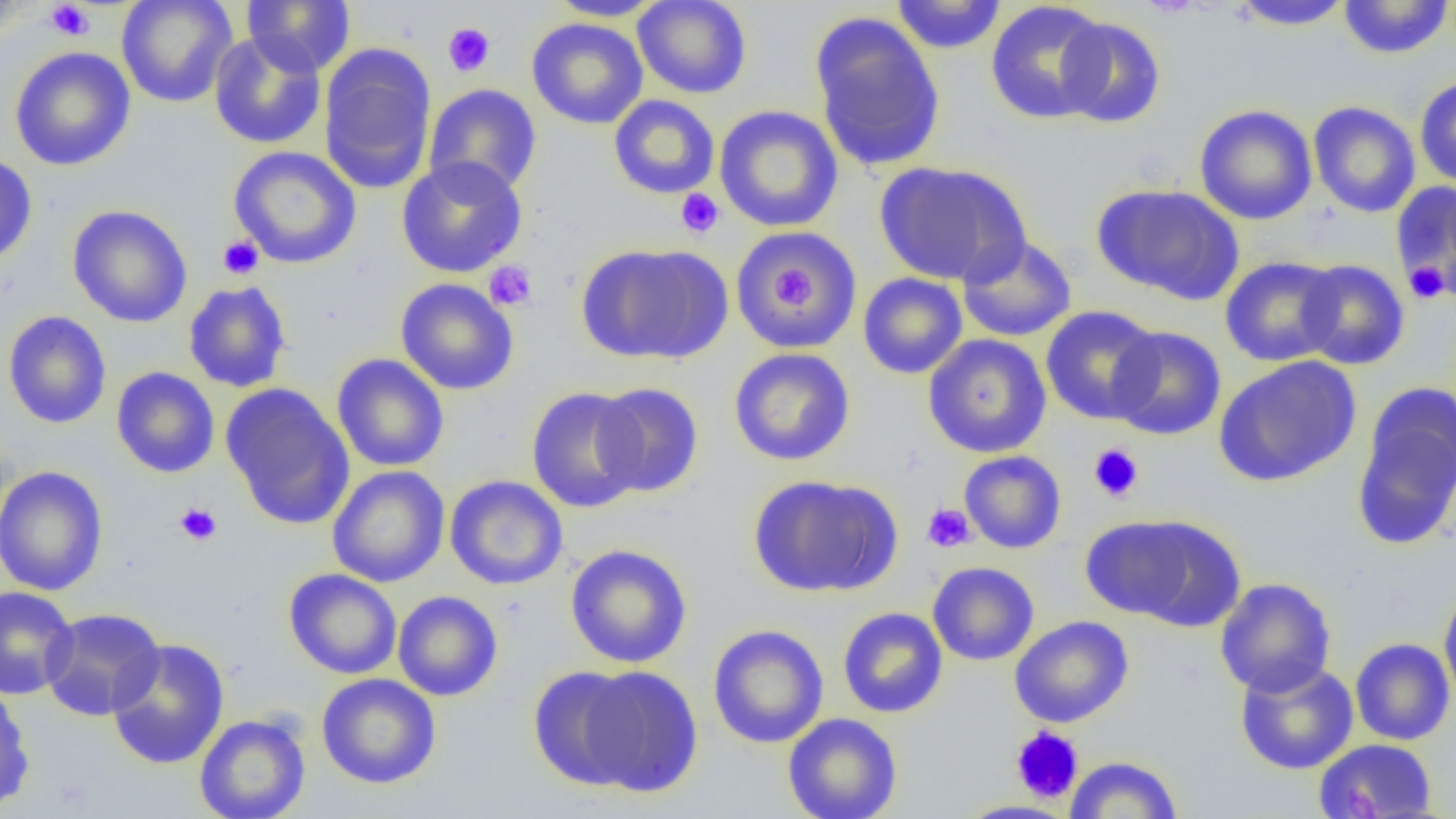

Summary:
  - Coordinate format: approximate bounding boxes as (x1, y1, x2, y2) in pixels
  - Platelet locations: (46, 1, 93, 40), (442, 22, 495, 77), (676, 188, 724, 238), (218, 235, 264, 279), (483, 260, 537, 310), (1403, 260, 1451, 305), (768, 263, 820, 317), (1088, 443, 1144, 502), (173, 502, 222, 546), (921, 503, 976, 553), (1010, 726, 1083, 803)
  - Uninfected red blood cell locations: (0, 0, 29, 44), (116, 0, 238, 108), (242, 0, 356, 76), (547, 0, 665, 21), (633, 0, 752, 99), (890, 0, 1007, 55), (1338, 0, 1453, 59), (985, 1, 1110, 124), (1230, 1, 1353, 32), (809, 12, 946, 172), (526, 17, 649, 129), (1055, 17, 1167, 128), (209, 31, 327, 149), (319, 44, 437, 192), (10, 47, 136, 171), (1414, 76, 1456, 189), (424, 84, 542, 197), (608, 95, 720, 199), (1308, 101, 1420, 218), (1194, 104, 1318, 225), (714, 105, 843, 233), (228, 145, 362, 269), (0, 154, 37, 269), (396, 156, 527, 278), (874, 161, 1030, 286), (1391, 181, 1456, 296), (1093, 184, 1245, 305), (67, 204, 193, 327), (732, 227, 863, 352), (957, 234, 1077, 342), (577, 243, 732, 364), (1219, 256, 1343, 367), (1297, 259, 1409, 370), (858, 273, 968, 379), (395, 278, 519, 395), (183, 281, 292, 393), (1040, 305, 1162, 425), (2, 310, 112, 429), (1107, 326, 1227, 441), (922, 333, 1052, 458), (728, 347, 856, 466), (332, 354, 449, 472), (1213, 355, 1362, 487), (111, 367, 220, 478), (592, 382, 705, 497), (220, 383, 356, 529), (1351, 383, 1456, 549), (526, 386, 647, 513), (959, 450, 1067, 554), (0, 465, 109, 597), (327, 466, 450, 587), (747, 474, 902, 598), (444, 475, 568, 590), (1078, 514, 1211, 624), (565, 544, 693, 668), (927, 561, 1039, 666), (284, 568, 402, 679), (1215, 577, 1337, 697), (0, 586, 79, 700), (1438, 586, 1456, 708), (392, 590, 503, 701), (40, 607, 165, 721), (837, 607, 948, 718), (1009, 615, 1134, 728), (707, 624, 829, 748), (1350, 637, 1455, 745), (106, 638, 230, 770), (1234, 659, 1359, 775), (572, 665, 702, 797), (527, 666, 648, 791), (316, 673, 441, 789), (0, 686, 35, 813), (194, 713, 311, 819), (782, 713, 903, 819), (1313, 738, 1438, 819), (1065, 755, 1183, 818), (956, 800, 1077, 819)
  - Slide-level diagnosis: negative for blood parasites
  - Image size: 1456×819 pixels
  - Magnification: 1000x
  - Field of view: single
  - Preparation: thin blood film
  - Modality: light microscopy